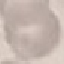

Malaria status: uninfected. Cell patch, automatically extracted from a larger field of view and resized to 64 × 64 pixels. Thin smear of blood. Giemsa stain. Acquired by smartphone through the microscope eyepiece.